Classify this cell by malaria status.
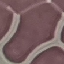
It is uninfected.

{
  "image_type": "automatically extracted cell patch, resized to 64 × 64 pixels",
  "preparation": "thin blood film",
  "stain": "Giemsa",
  "capture": "smartphone through the microscope eyepiece"
}